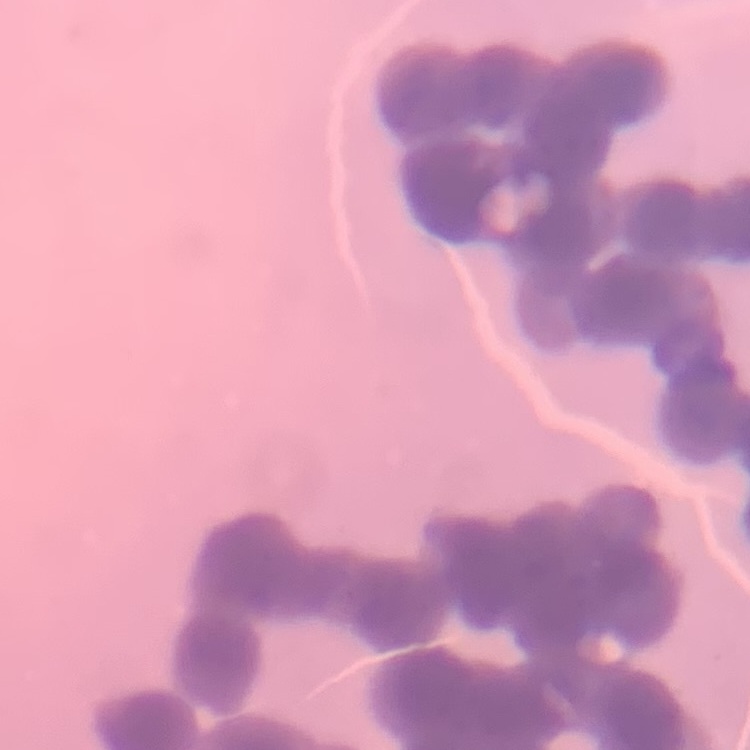

erythrocyte morphology = rouleaux formation
stain = Field's or Giemsa
image type = one tile cut from a larger photomicrograph
preparation = thin blood smear